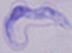

Summary:
  - Modality: photomicrograph
  - Identification: trypanosome
  - Magnification: 1000x